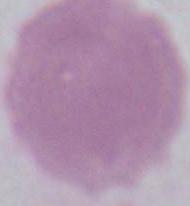
magnification = 1000x
identification = red blood cell
modality = micrograph